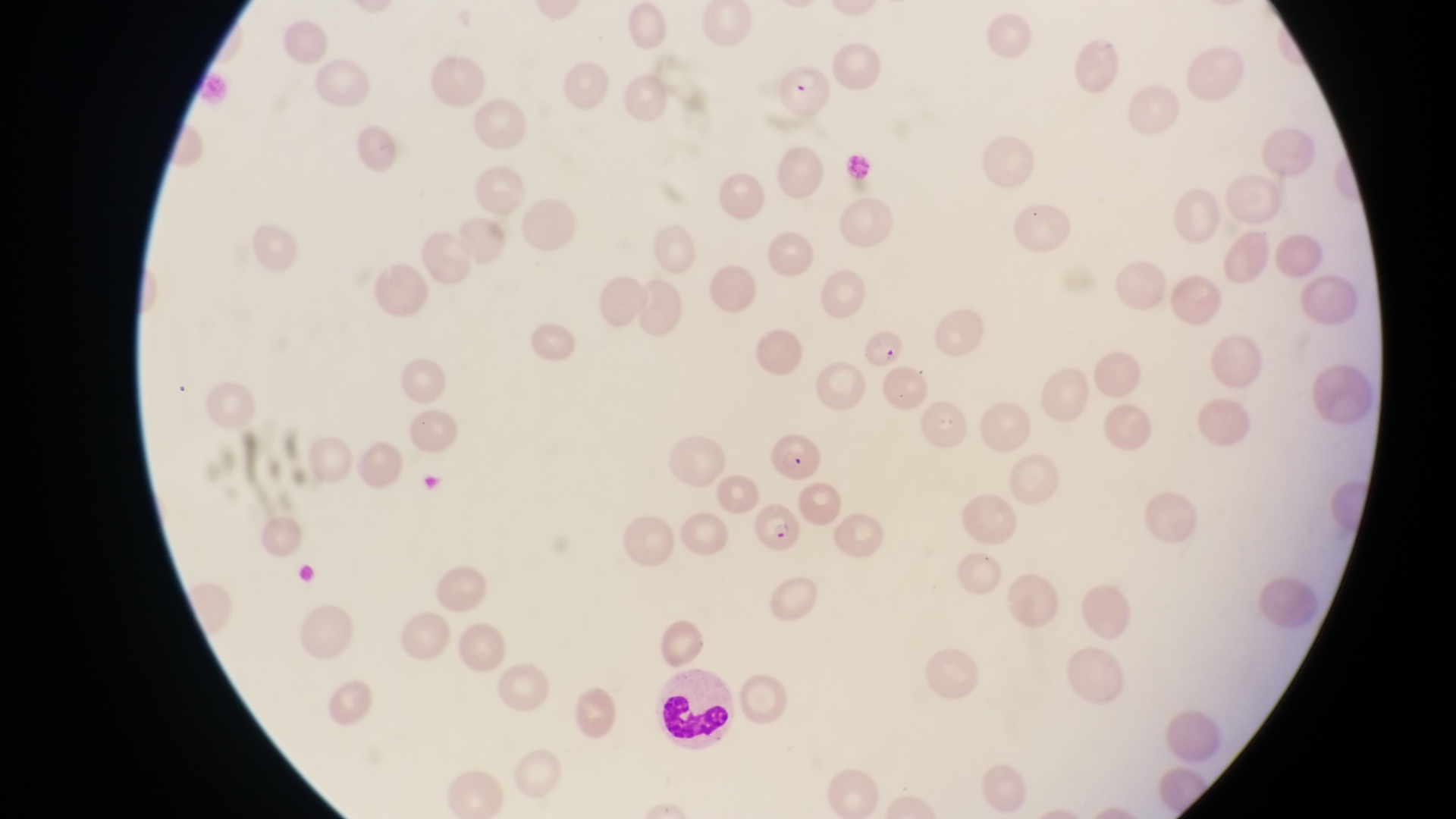 Approximate bounding boxes as {left, top, right, bottom} in pixels. Parasitised red blood cell locations: {774, 60, 827, 110}, {865, 331, 910, 373}, {772, 433, 819, 480}, {753, 497, 809, 557}. Leukocyte locations: {657, 667, 739, 747}. Photographed through the eyepiece of an Olympus CX-23 microscope with a smartphone camera. Image is 1456×819 pixels. At a magnification of 1000x. Thin blood film. One field of view. Collected in Uganda.